Report the malaria status of this cell.
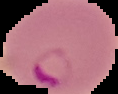

Parasitized.

Cell region segmented out of the field of view; the surrounding area is masked to black. From a thin blood smear. Image is 118×94 pixels.